Assess this cell for malaria.
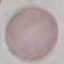

It is uninfected.

Acquired by smartphone through the microscope eyepiece. Cell patch, automatically extracted from a larger field of view and resized to 64 × 64 pixels. Thin blood smear. Giemsa stain.